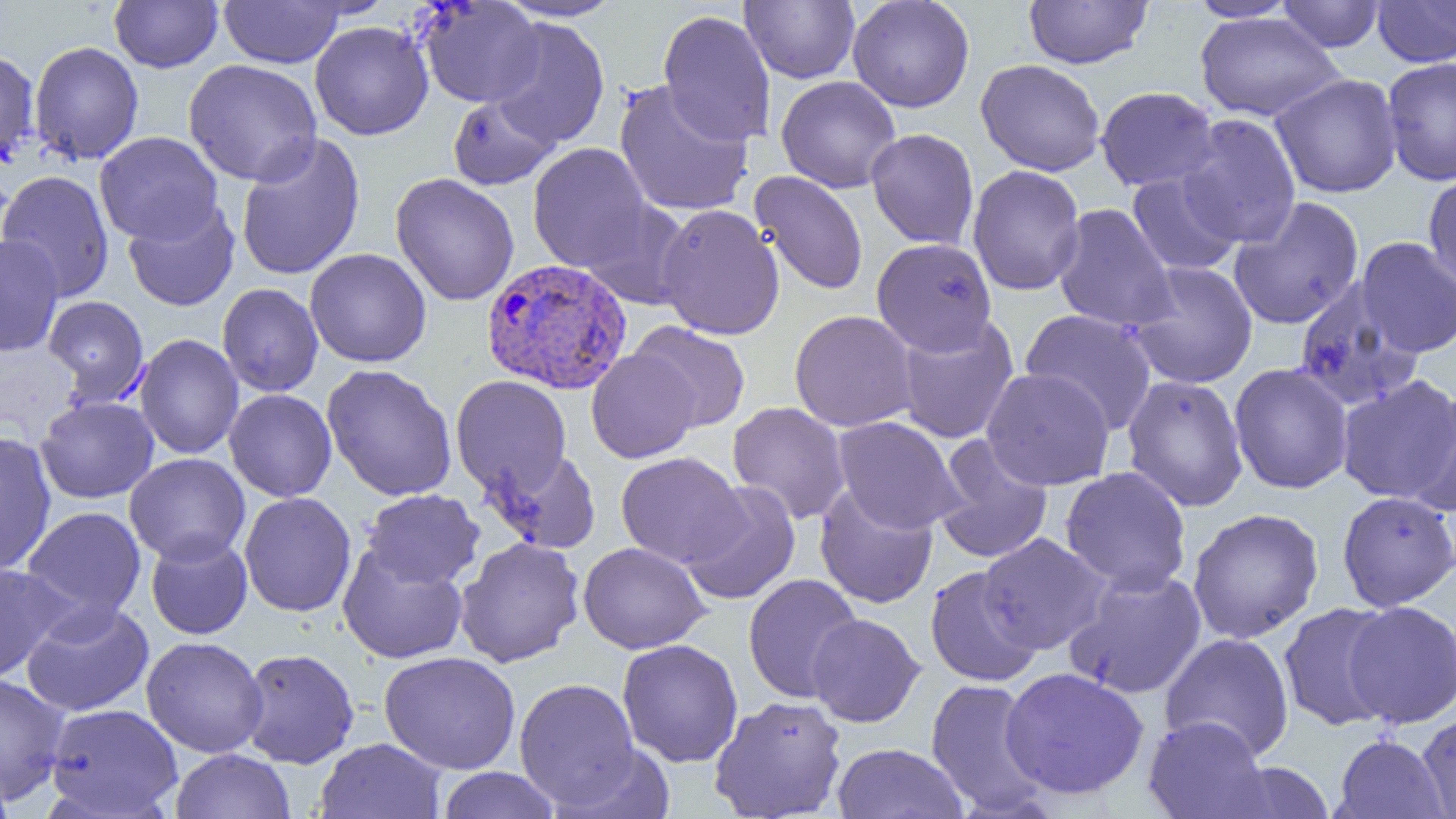

Approximate bounding boxes as (x1, y1, x2, y2) in pixels. Uninfected red blood cell locations: (109, 0, 223, 73), (220, 0, 345, 68), (496, 0, 628, 22), (740, 0, 859, 84), (847, 0, 975, 113), (1024, 0, 1153, 69), (1186, 0, 1301, 22), (1372, 0, 1456, 67), (416, 1, 544, 108), (1277, 1, 1385, 52), (657, 9, 776, 147), (1195, 13, 1344, 122), (488, 16, 610, 150), (309, 20, 434, 140), (28, 40, 144, 165), (0, 48, 40, 169), (1381, 56, 1456, 186), (183, 59, 322, 186), (975, 59, 1105, 176), (1270, 73, 1403, 198), (776, 75, 902, 193), (613, 80, 754, 217), (1094, 86, 1220, 192), (448, 93, 559, 190), (1177, 114, 1302, 248), (865, 128, 980, 250), (94, 131, 222, 245), (235, 131, 366, 282), (527, 143, 653, 273), (967, 165, 1086, 296), (0, 169, 115, 302), (750, 171, 868, 296), (1126, 171, 1244, 277), (1423, 172, 1456, 289), (390, 173, 520, 307), (1229, 197, 1365, 330), (578, 198, 695, 310), (122, 199, 240, 311), (1052, 203, 1178, 333), (656, 204, 785, 340), (0, 234, 65, 357), (871, 237, 997, 356), (1356, 237, 1456, 358), (304, 248, 432, 368), (1127, 261, 1259, 389), (1293, 280, 1424, 412), (217, 283, 323, 397), (42, 295, 150, 404), (1020, 309, 1158, 434), (788, 310, 918, 432), (895, 315, 1019, 443), (628, 321, 752, 433), (134, 334, 244, 460), (586, 349, 702, 464), (1229, 363, 1354, 494), (321, 364, 458, 501), (981, 367, 1115, 490), (1121, 374, 1249, 511), (450, 375, 571, 497), (1336, 375, 1456, 505), (1404, 387, 1456, 519), (224, 389, 337, 502), (34, 396, 159, 503), (727, 401, 851, 525), (832, 416, 966, 534), (0, 431, 57, 577), (931, 435, 1054, 565), (483, 447, 602, 554), (615, 452, 748, 569), (124, 453, 250, 566), (1059, 467, 1192, 595), (679, 481, 800, 606), (814, 484, 939, 609), (361, 489, 485, 589), (239, 491, 357, 617), (1337, 491, 1456, 612), (22, 506, 146, 622), (1186, 507, 1324, 644), (978, 533, 1112, 654), (145, 534, 252, 640), (455, 537, 585, 667), (578, 541, 711, 654), (337, 544, 468, 664), (0, 562, 74, 683), (925, 565, 1045, 687), (1063, 568, 1207, 699), (743, 573, 864, 703), (21, 600, 154, 717), (1342, 600, 1456, 728), (1278, 602, 1398, 732), (806, 613, 925, 727), (1159, 632, 1295, 761), (141, 636, 268, 758), (617, 638, 743, 767), (238, 648, 359, 768), (379, 651, 520, 774), (1000, 666, 1149, 800), (0, 673, 71, 806), (514, 677, 641, 810), (925, 678, 1050, 815), (709, 695, 848, 819), (44, 703, 183, 818), (1417, 710, 1456, 819), (1143, 715, 1273, 819), (1332, 734, 1449, 819), (315, 737, 447, 819), (552, 742, 678, 819), (831, 743, 967, 818), (170, 748, 296, 819), (1220, 761, 1337, 818), (0, 767, 15, 819), (435, 767, 562, 819). Plasmodium vivax-infected red blood cell locations: (480, 258, 633, 395). Slide-level diagnosis: Plasmodium vivax. Thin blood smear. Optical microscopy. One field of a larger specimen. Captured at 1000x magnification. Image is 1456×819 pixels.